Report the malaria status of this cell.
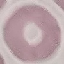
It is uninfected.

capture = smartphone camera at the microscope eyepiece
preparation = thin blood smear
image type = cell patch, automatically extracted from a larger field of view and resized to 64 × 64 pixels
stain = Giemsa